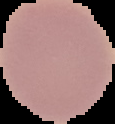

image type = segmented cell region with the area outside set to black
preparation = thin blood film
malaria status = uninfected
image size = 115×124 pixels